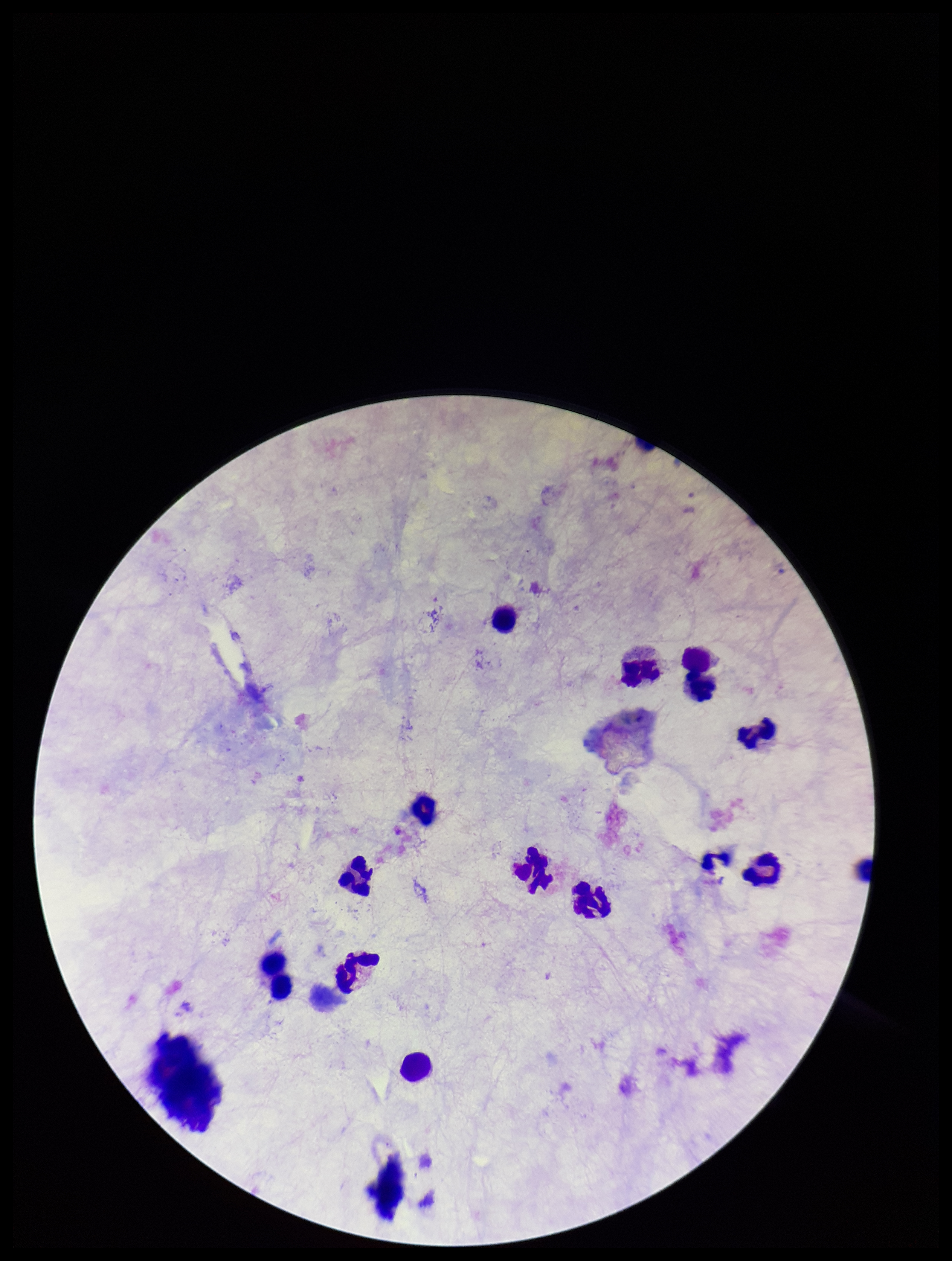

Plasmodium parasites = none identified
stain = Giemsa
image size = 952×1261 pixels
leukocyte count = 12
preparation = thick
capture = smartphone photograph through the microscope eyepiece
patient malaria status = negative
field of view = one from this slide
parasite count = 0